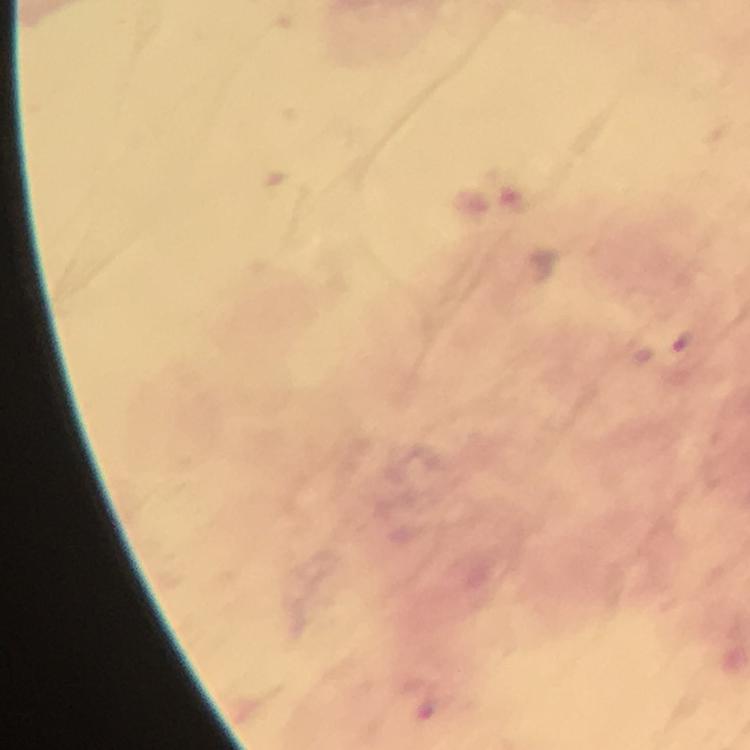
Approximate object centers, in pixels from the top-left corner. Malaria parasite locations: (x=680, y=341). Image is 750×750 pixels. Thick smear. Giemsa stain. From a diagnostic examination for malaria. Immersion oil applied. 100x magnification. Smartphone photograph taken through a microscope. Cropped region of a single field of view.